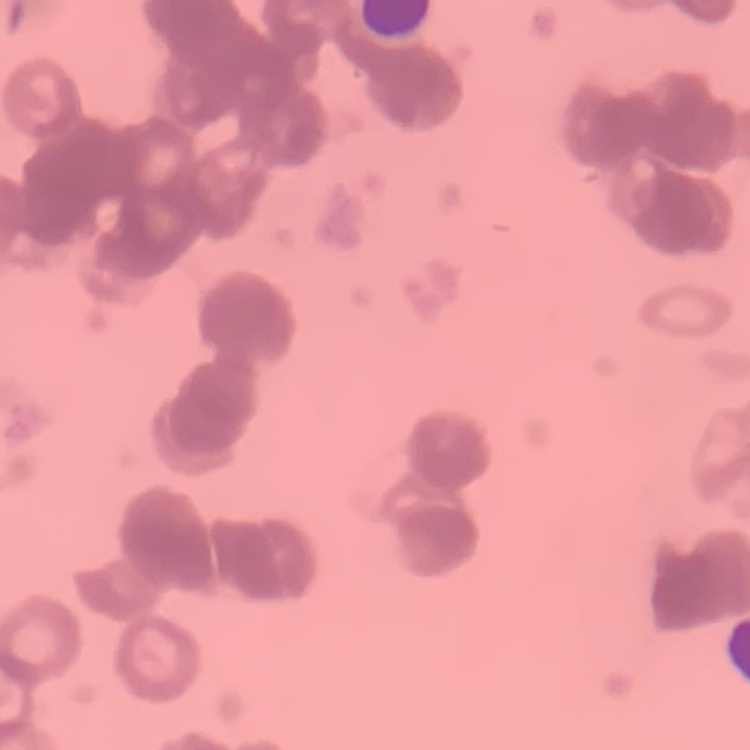
Summary:
  - Erythrocyte morphology: rouleaux formation
  - Image type: one tile cut from a larger photomicrograph
  - Preparation: thin blood film
  - Stain: Field's or Giemsa